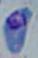

Summary:
  - Identification: Toxoplasma gondii
  - Modality: photomicrograph
  - Magnification: 1000x